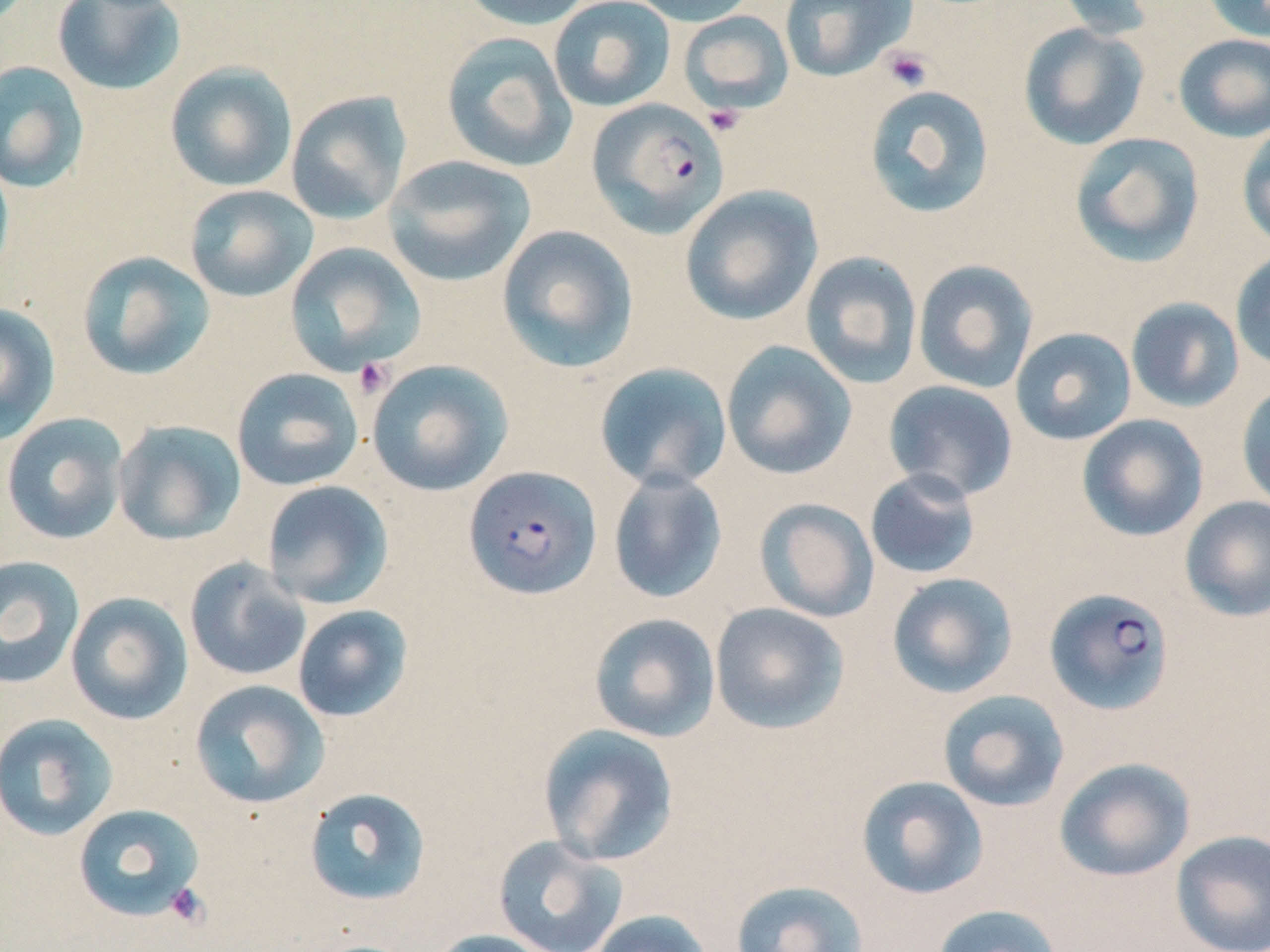

Approximate bounding boxes as named x1/y1/x2/y2 corners in pixels. Uninfected red blood cell locations: (x1=457, y1=0, x2=595, y2=31), (x1=548, y1=0, x2=676, y2=113), (x1=625, y1=0, x2=759, y2=26), (x1=778, y1=0, x2=917, y2=82), (x1=1053, y1=0, x2=1160, y2=39), (x1=1200, y1=0, x2=1270, y2=42), (x1=52, y1=1, x2=186, y2=96), (x1=678, y1=11, x2=794, y2=116), (x1=1018, y1=22, x2=1149, y2=150), (x1=441, y1=32, x2=578, y2=173), (x1=1174, y1=33, x2=1270, y2=142), (x1=0, y1=61, x2=89, y2=194), (x1=164, y1=62, x2=298, y2=192), (x1=862, y1=84, x2=995, y2=219), (x1=285, y1=90, x2=412, y2=225), (x1=1236, y1=123, x2=1270, y2=252), (x1=1069, y1=132, x2=1205, y2=267), (x1=0, y1=154, x2=14, y2=287), (x1=382, y1=155, x2=536, y2=287), (x1=184, y1=185, x2=318, y2=302), (x1=680, y1=185, x2=823, y2=326), (x1=496, y1=225, x2=639, y2=373), (x1=284, y1=242, x2=426, y2=377), (x1=76, y1=250, x2=216, y2=381), (x1=1230, y1=250, x2=1270, y2=374), (x1=800, y1=251, x2=923, y2=389), (x1=912, y1=260, x2=1039, y2=394), (x1=1126, y1=297, x2=1244, y2=413), (x1=0, y1=303, x2=61, y2=446), (x1=1009, y1=327, x2=1137, y2=445), (x1=721, y1=340, x2=857, y2=480), (x1=366, y1=359, x2=513, y2=496), (x1=594, y1=362, x2=732, y2=492), (x1=231, y1=367, x2=364, y2=492), (x1=883, y1=380, x2=1018, y2=502), (x1=1236, y1=384, x2=1270, y2=513), (x1=1, y1=412, x2=129, y2=545), (x1=1077, y1=414, x2=1208, y2=542), (x1=113, y1=419, x2=246, y2=545), (x1=607, y1=469, x2=728, y2=604), (x1=864, y1=469, x2=982, y2=580), (x1=261, y1=480, x2=394, y2=610), (x1=1179, y1=496, x2=1270, y2=622), (x1=754, y1=498, x2=880, y2=623), (x1=0, y1=555, x2=86, y2=690), (x1=184, y1=557, x2=311, y2=682), (x1=886, y1=572, x2=1018, y2=699), (x1=65, y1=591, x2=193, y2=725), (x1=709, y1=602, x2=850, y2=735), (x1=292, y1=604, x2=414, y2=723), (x1=588, y1=613, x2=721, y2=743), (x1=189, y1=679, x2=329, y2=810), (x1=937, y1=689, x2=1070, y2=813), (x1=0, y1=713, x2=119, y2=841), (x1=537, y1=724, x2=680, y2=866), (x1=1053, y1=757, x2=1196, y2=883), (x1=855, y1=775, x2=989, y2=900), (x1=303, y1=786, x2=432, y2=907), (x1=72, y1=802, x2=206, y2=922), (x1=1170, y1=830, x2=1270, y2=952), (x1=493, y1=834, x2=629, y2=952), (x1=730, y1=879, x2=869, y2=952), (x1=931, y1=903, x2=1063, y2=952), (x1=587, y1=908, x2=714, y2=952), (x1=425, y1=928, x2=563, y2=952). Platelet locations: (x1=882, y1=47, x2=934, y2=93), (x1=702, y1=104, x2=746, y2=137), (x1=353, y1=357, x2=393, y2=399), (x1=164, y1=883, x2=211, y2=928). Plasmodium falciparum-infected red blood cell locations: (x1=587, y1=97, x2=730, y2=239), (x1=463, y1=465, x2=602, y2=600), (x1=1044, y1=587, x2=1175, y2=715). Slide-level diagnosis: Plasmodium falciparum. 1000x magnification. May-Grünwald-Giemsa stain. Optical microscopy. Image is 1270×952 pixels. Thin blood smear. Single field of view.